Assess this cell for malaria.
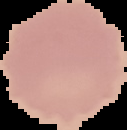
It is uninfected.

Summary:
  - Image size: 127×130 pixels
  - Preparation: thin blood film
  - Image type: segmented cell region on a black background